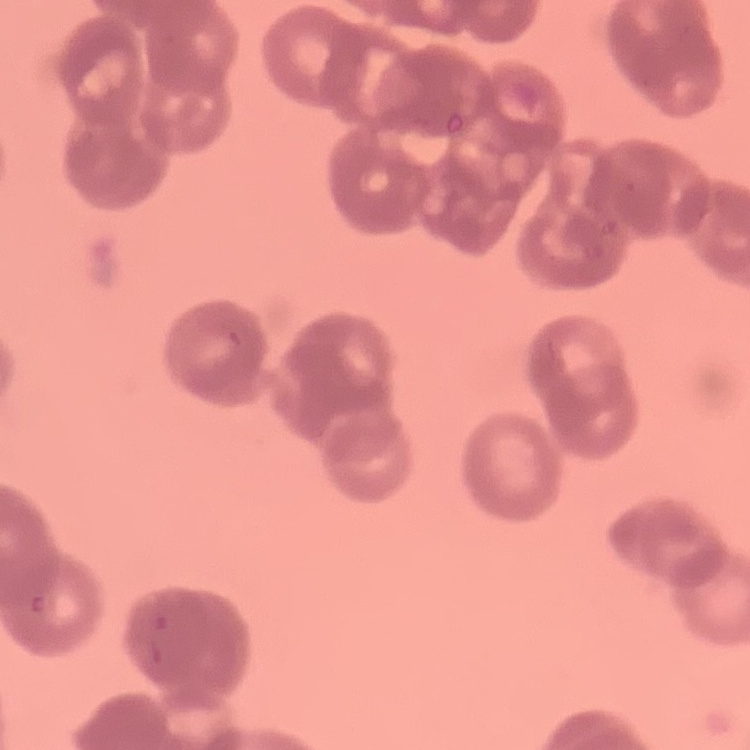

Summary:
  - Red blood cell morphology: rouleaux formation
  - Image type: one tile cut from a larger photomicrograph
  - Stain: Field's or Giemsa
  - Preparation: thin blood film